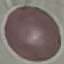
result = no malaria parasites detected
stain = Giemsa
image type = automatically extracted cell patch, resized to 64 × 64 pixels
capture = smartphone through the microscope eyepiece
preparation = thin blood smear